Assess this cell for malaria.
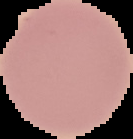
Uninfected.

From a thin blood smear. Cell region segmented out of the field of view; the surrounding area is masked to black. Image is 133×139 pixels.